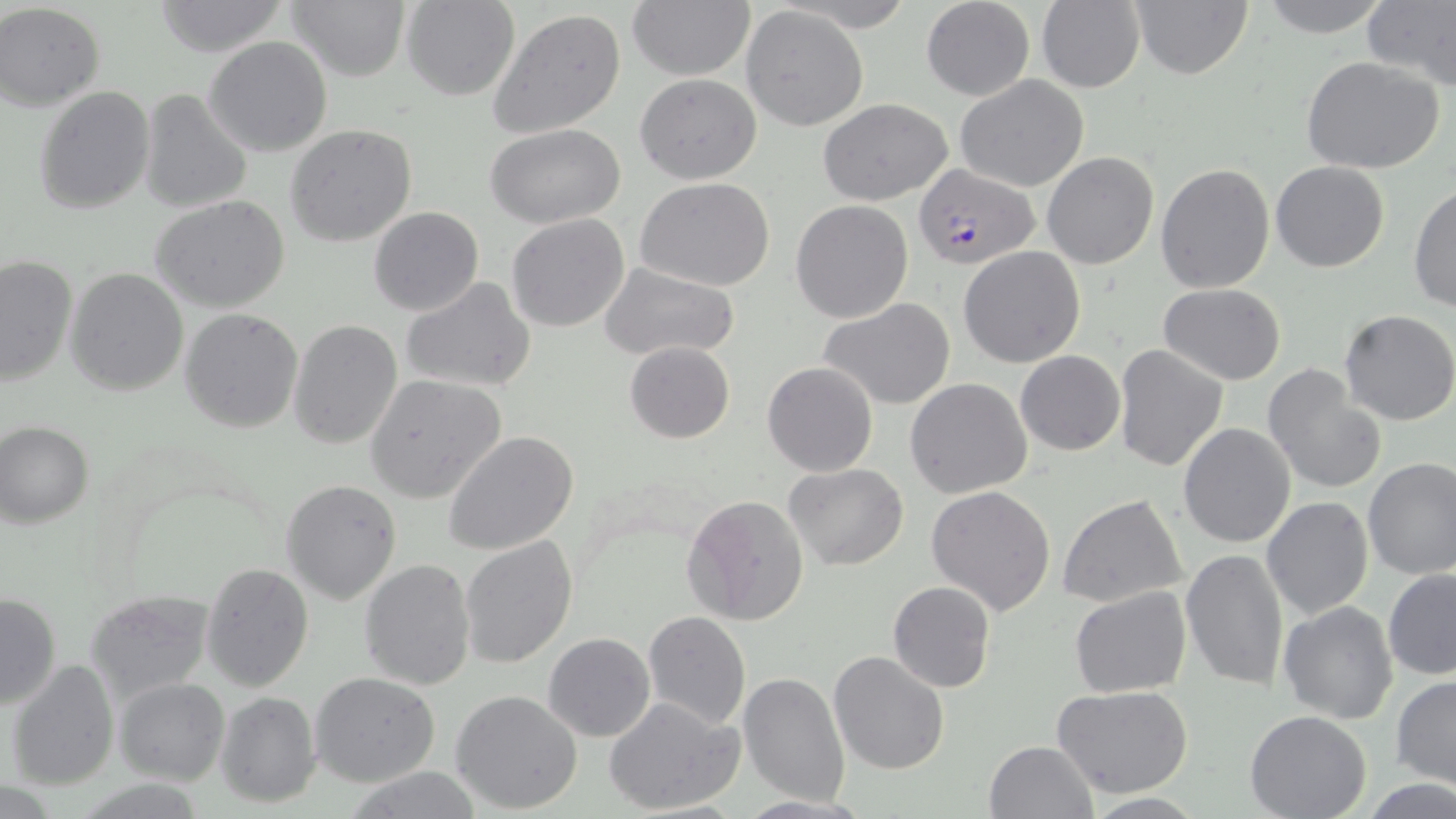
Summary:
  - Coordinate format: approximate bounding boxes as named x1/y1/x2/y2 corners in pixels
  - Uninfected red blood cell locations: (x1=286, y1=0, x2=411, y2=81), (x1=627, y1=0, x2=756, y2=80), (x1=920, y1=0, x2=1035, y2=100), (x1=1254, y1=0, x2=1396, y2=38), (x1=153, y1=1, x2=289, y2=55), (x1=400, y1=1, x2=520, y2=99), (x1=1130, y1=1, x2=1252, y2=79), (x1=1363, y1=1, x2=1456, y2=90), (x1=1, y1=2, x2=105, y2=110), (x1=1036, y1=2, x2=1145, y2=92), (x1=741, y1=5, x2=868, y2=131), (x1=488, y1=9, x2=627, y2=140), (x1=204, y1=37, x2=333, y2=156), (x1=1300, y1=56, x2=1446, y2=173), (x1=634, y1=73, x2=762, y2=185), (x1=956, y1=74, x2=1090, y2=192), (x1=33, y1=86, x2=156, y2=214), (x1=138, y1=90, x2=252, y2=213), (x1=817, y1=98, x2=954, y2=204), (x1=286, y1=125, x2=418, y2=247), (x1=485, y1=125, x2=628, y2=229), (x1=1042, y1=152, x2=1158, y2=270), (x1=1271, y1=161, x2=1391, y2=273), (x1=1154, y1=163, x2=1275, y2=293), (x1=636, y1=178, x2=775, y2=291), (x1=1410, y1=186, x2=1456, y2=314), (x1=152, y1=195, x2=292, y2=314), (x1=790, y1=201, x2=913, y2=323), (x1=369, y1=206, x2=483, y2=315), (x1=506, y1=214, x2=632, y2=332), (x1=959, y1=246, x2=1086, y2=368), (x1=1, y1=253, x2=77, y2=387), (x1=600, y1=263, x2=739, y2=362), (x1=64, y1=267, x2=190, y2=396), (x1=399, y1=277, x2=536, y2=392), (x1=1159, y1=282, x2=1286, y2=385), (x1=819, y1=299, x2=955, y2=409), (x1=179, y1=308, x2=304, y2=433), (x1=1340, y1=310, x2=1456, y2=426), (x1=288, y1=319, x2=403, y2=450), (x1=625, y1=340, x2=733, y2=443), (x1=1114, y1=343, x2=1228, y2=471), (x1=1015, y1=350, x2=1124, y2=455), (x1=762, y1=362, x2=879, y2=477), (x1=1262, y1=365, x2=1387, y2=495), (x1=365, y1=375, x2=507, y2=502), (x1=905, y1=377, x2=1033, y2=498), (x1=1, y1=422, x2=94, y2=527), (x1=1177, y1=422, x2=1296, y2=548), (x1=444, y1=430, x2=579, y2=555), (x1=1361, y1=457, x2=1456, y2=581), (x1=785, y1=463, x2=909, y2=569), (x1=281, y1=479, x2=401, y2=606), (x1=925, y1=483, x2=1057, y2=617), (x1=1058, y1=493, x2=1188, y2=608), (x1=683, y1=494, x2=810, y2=625), (x1=1262, y1=497, x2=1374, y2=620), (x1=459, y1=535, x2=577, y2=667), (x1=1179, y1=547, x2=1289, y2=691), (x1=359, y1=559, x2=476, y2=691), (x1=202, y1=561, x2=315, y2=692), (x1=1384, y1=566, x2=1456, y2=679), (x1=888, y1=581, x2=995, y2=693), (x1=1069, y1=587, x2=1191, y2=697), (x1=84, y1=588, x2=215, y2=702), (x1=1, y1=592, x2=61, y2=710), (x1=1279, y1=599, x2=1399, y2=724), (x1=643, y1=611, x2=751, y2=729), (x1=543, y1=632, x2=656, y2=741), (x1=827, y1=650, x2=951, y2=774), (x1=6, y1=659, x2=120, y2=790), (x1=738, y1=672, x2=851, y2=807), (x1=310, y1=674, x2=439, y2=788), (x1=1391, y1=676, x2=1456, y2=790), (x1=114, y1=678, x2=229, y2=785), (x1=1049, y1=685, x2=1195, y2=799), (x1=450, y1=689, x2=583, y2=812), (x1=214, y1=692, x2=319, y2=808), (x1=605, y1=696, x2=743, y2=817), (x1=1244, y1=711, x2=1371, y2=819), (x1=984, y1=740, x2=1097, y2=819), (x1=343, y1=766, x2=486, y2=818)
  - Plasmodium falciparum-infected red blood cell locations: (x1=915, y1=164, x2=1038, y2=269)
  - Slide-level diagnosis: Plasmodium falciparum
  - Preparation: thin blood smear
  - Stain: May-Grünwald-Giemsa
  - Field of view: one of a larger specimen
  - Image size: 1456×819 pixels
  - Modality: optical microscopy
  - Magnification: 1000x